Point out every malaria parasite and every leukocyte.
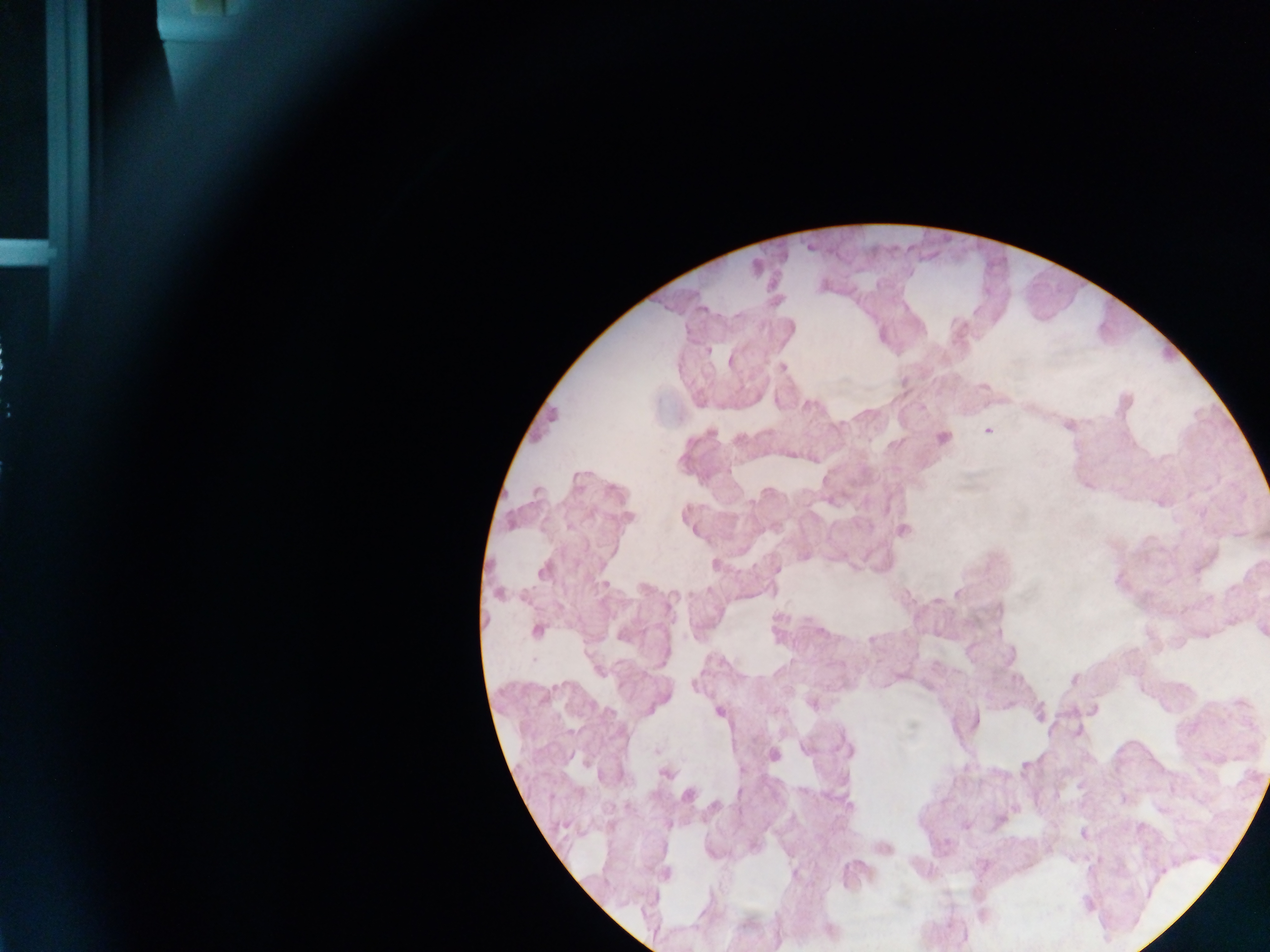

Approximate centers as x y in pixels.
Malaria parasites: 708 350; 782 367; 1124 402; 1067 424; 988 430; 941 438; 1160 501; 628 517; 902 529; 715 564; 777 568; 543 570; 498 593; 1261 630; 536 631; 1073 678; 812 702; 1092 709; 719 711; 1077 733; 806 748; 772 755; 666 772; 687 794; 965 826; 1083 834; 883 848; 665 875; 829 931.
No leukocytes observed.

Thick blood smear. Collected in Ghana. One field of view. Image is 1270×952 pixels. Photographed through a microscope with a mobile-phone camera.